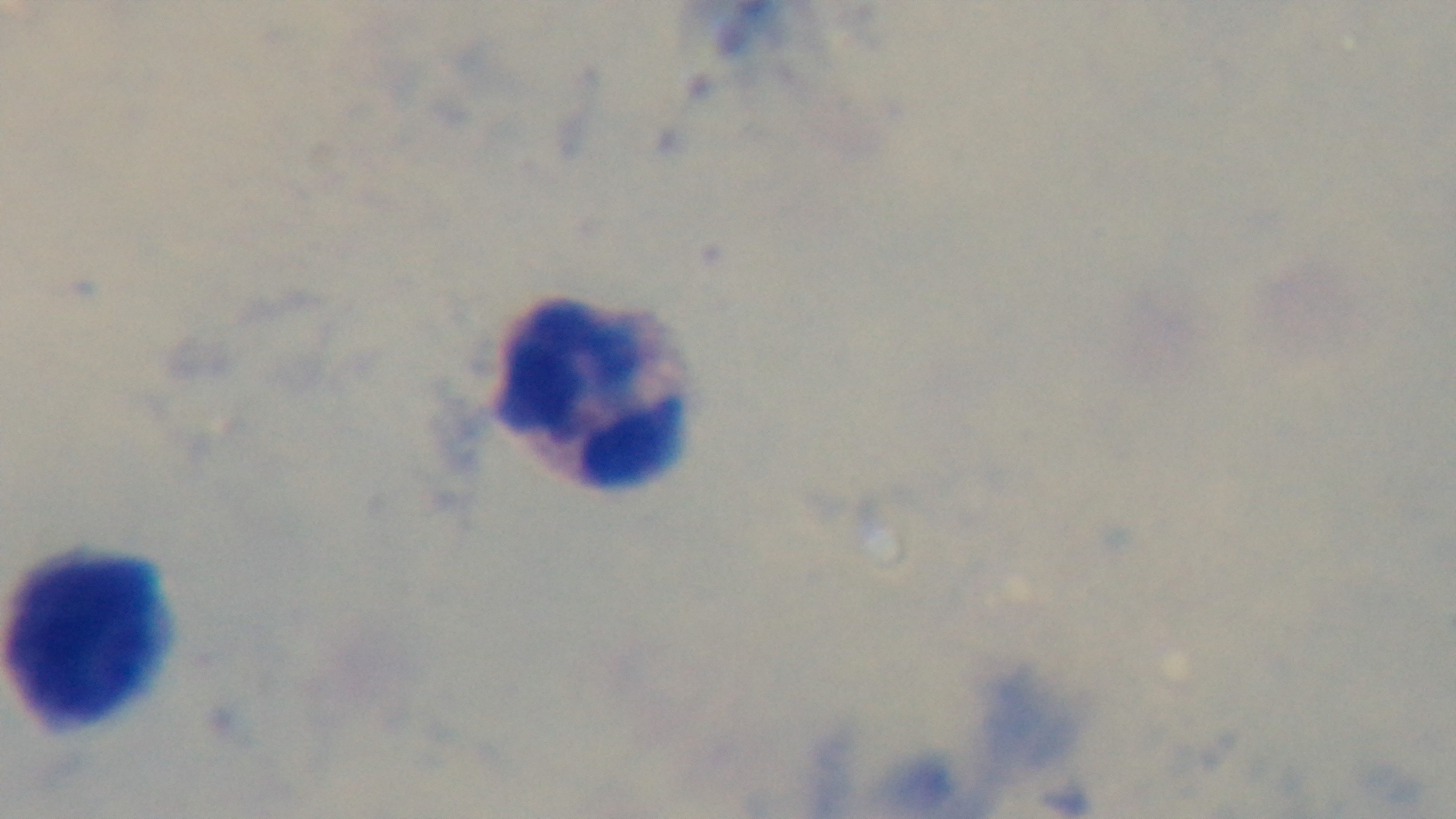

field of view = one from the slide
capture = mounted 4K digital camera
preparation = thick
stain = Giemsa
malaria status = uninfected
objective = 100x oil immersion
modality = light microscopy